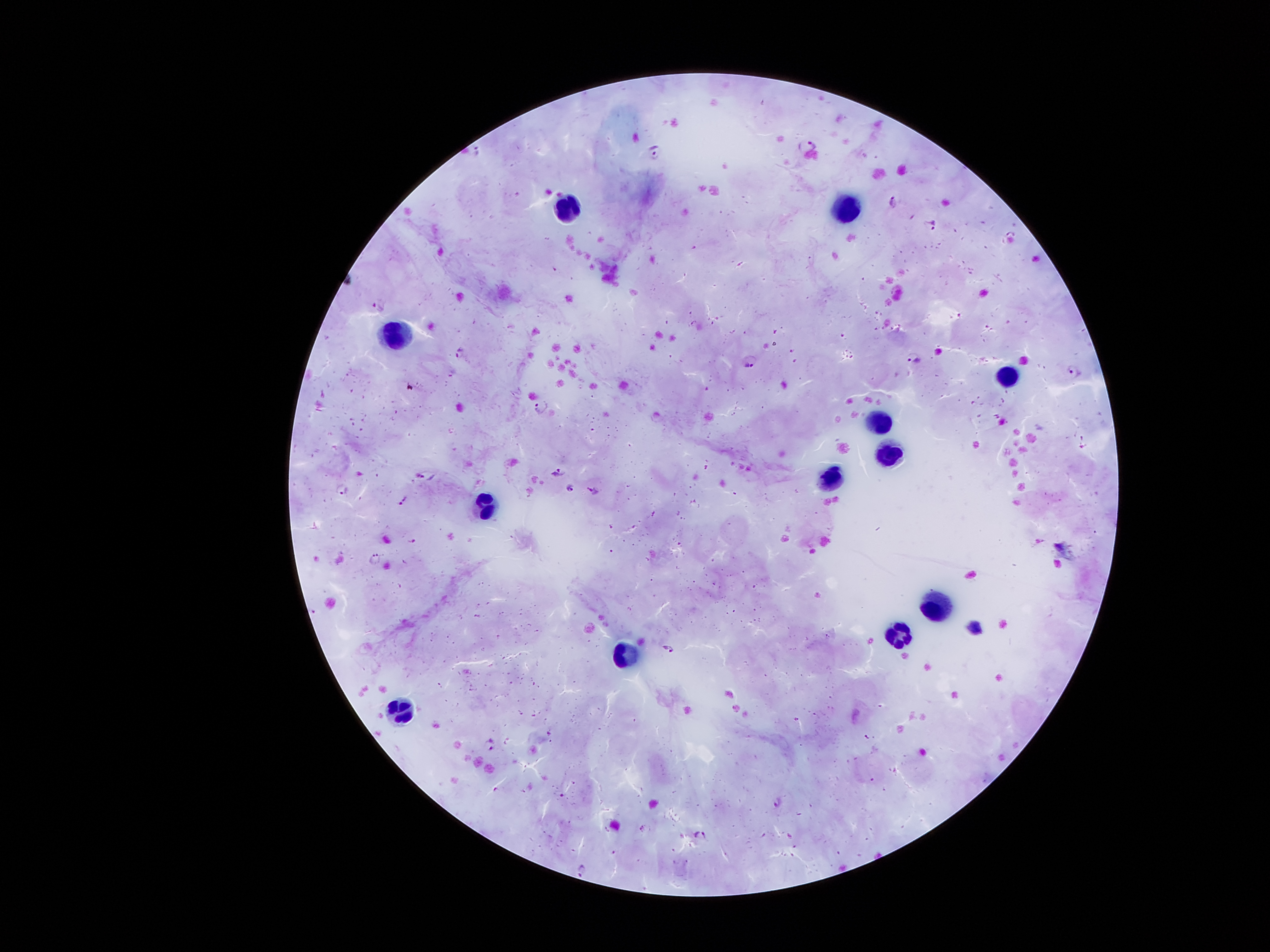

coordinate format = approximate object centers, in pixels from the top-left corner
leukocyte locations = (x=850, y=207), (x=569, y=210), (x=400, y=334), (x=1007, y=379), (x=876, y=422), (x=891, y=451), (x=831, y=485), (x=486, y=510), (x=938, y=607), (x=899, y=636), (x=628, y=656), (x=398, y=705)
Plasmodium parasite locations = (x=810, y=146), (x=654, y=152), (x=893, y=199), (x=926, y=228), (x=380, y=301), (x=460, y=350), (x=915, y=355), (x=748, y=360), (x=1073, y=370), (x=542, y=404), (x=559, y=472), (x=570, y=487), (x=344, y=490), (x=595, y=491), (x=402, y=498), (x=373, y=559), (x=670, y=651), (x=490, y=745), (x=778, y=803), (x=643, y=830), (x=701, y=835), (x=583, y=867)
field of view = one from this slide
stain = Giemsa
preparation = thick peripheral-blood smear
magnification = 100x
image size = 1270×952 pixels
capture = smartphone camera through the microscope eyepiece
patient malaria status = infected with Plasmodium falciparum